Assess this cell for malaria.
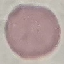

Uninfected.

Automatically extracted cell patch, resized to 64 × 64 pixels. Photographed with a smartphone camera at the microscope eyepiece. Thin smear of blood. Giemsa-stained preparation.